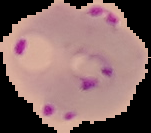

image_type: segmented cell region on a black background
image_size: 151×133 pixels
preparation: thin blood film
result: Plasmodium parasites identified